Assess the morphology of the red blood cells.
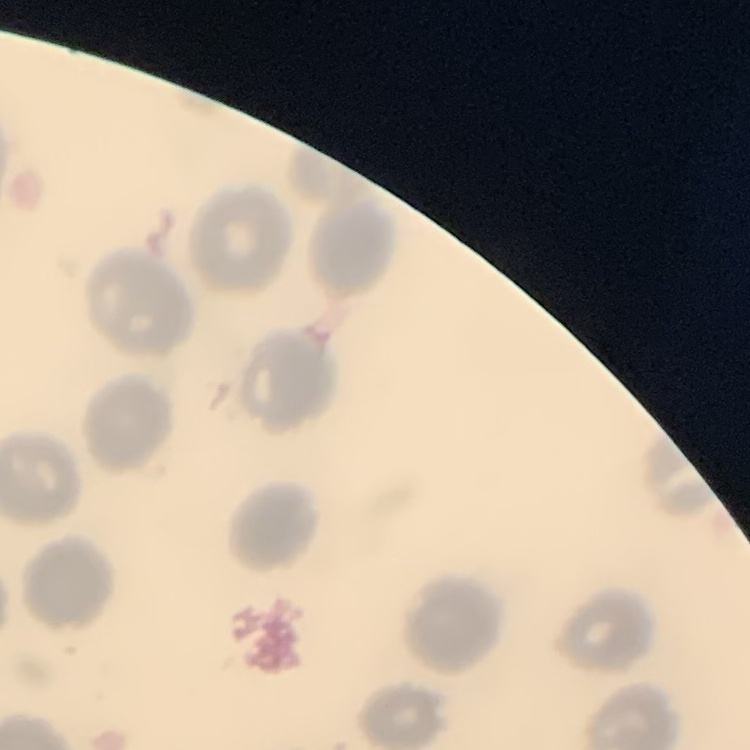

No rouleaux formation.

Summary:
  - Image type: one tile cut from a larger photomicrograph
  - Preparation: thin blood smear
  - Stain: Field's or Giemsa